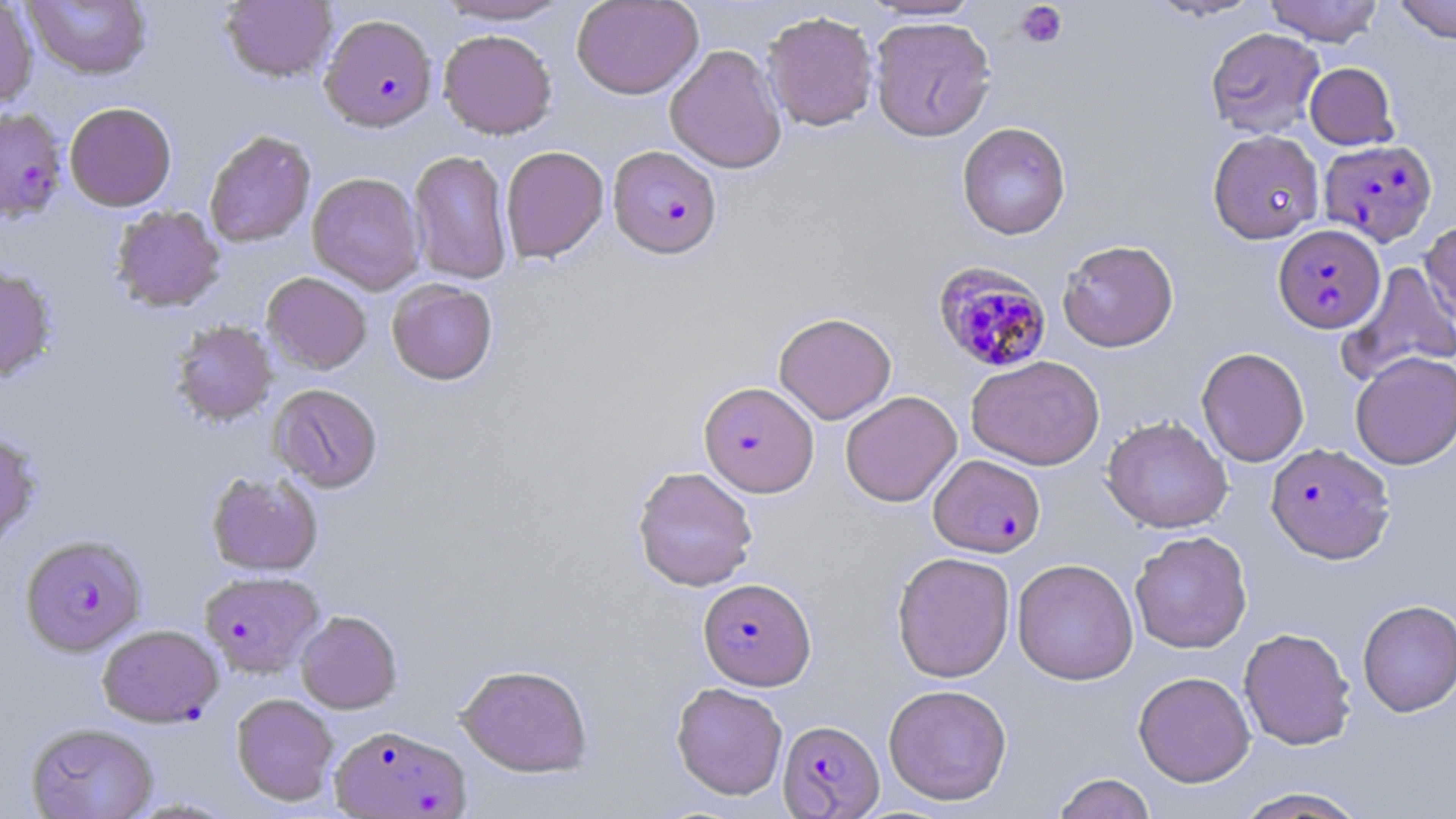
Summary:
  - Coordinate format: approximate bounding boxes as (x1, y1, x2, y2) in pixels
  - Uninfected red blood cell locations (subset): (23, 0, 152, 79), (220, 0, 338, 83), (435, 0, 574, 24), (571, 0, 703, 99), (862, 0, 984, 21), (1145, 0, 1265, 21), (1264, 0, 1384, 46), (1392, 0, 1456, 44), (0, 1, 38, 109), (761, 10, 879, 132), (869, 16, 996, 142), (1206, 27, 1325, 138), (438, 29, 557, 139), (664, 44, 787, 174), (1305, 62, 1398, 150), (64, 102, 177, 212), (957, 121, 1072, 240), (203, 129, 316, 248), (1207, 130, 1324, 244), (500, 146, 608, 263), (408, 149, 513, 284), (307, 172, 425, 294), (110, 205, 225, 313), (1420, 218, 1456, 331), (1057, 239, 1179, 352), (1339, 261, 1456, 385), (0, 266, 58, 383), (262, 272, 372, 374), (386, 279, 498, 385), (773, 311, 896, 424), (171, 320, 277, 426), (1196, 347, 1310, 467), (1350, 352, 1456, 469), (966, 355, 1105, 470), (269, 384, 383, 493), (840, 390, 962, 507), (1101, 415, 1233, 533), (0, 430, 42, 550), (632, 466, 759, 592), (206, 470, 323, 576), (1130, 530, 1252, 654), (891, 551, 1015, 683), (1012, 558, 1139, 685), (1357, 599, 1456, 716), (296, 610, 403, 714), (1238, 627, 1357, 751), (455, 663, 594, 777), (1133, 671, 1255, 787), (671, 681, 788, 800), (884, 683, 1012, 806), (231, 693, 339, 806), (25, 721, 159, 819), (1052, 772, 1157, 819), (1232, 787, 1369, 818)
  - Plasmodium falciparum-infected red blood cell locations (subset): (319, 13, 438, 133), (1319, 139, 1437, 246), (608, 145, 723, 260), (1273, 224, 1386, 334), (933, 262, 1052, 373), (700, 381, 819, 497), (1266, 443, 1395, 564), (928, 454, 1045, 558), (20, 533, 147, 656), (199, 570, 324, 679), (698, 577, 816, 690), (97, 624, 223, 727), (777, 719, 884, 818), (329, 724, 470, 818)
  - Platelet locations: (1015, 2, 1067, 49)
  - Slide-level diagnosis: Plasmodium falciparum
  - Field of view: single
  - Preparation: thin blood smear
  - Modality: light microscopy
  - Image size: 1456×819 pixels
  - Stain: May-Grünwald-Giemsa
  - Magnification: 1000x